Assess the background quality.
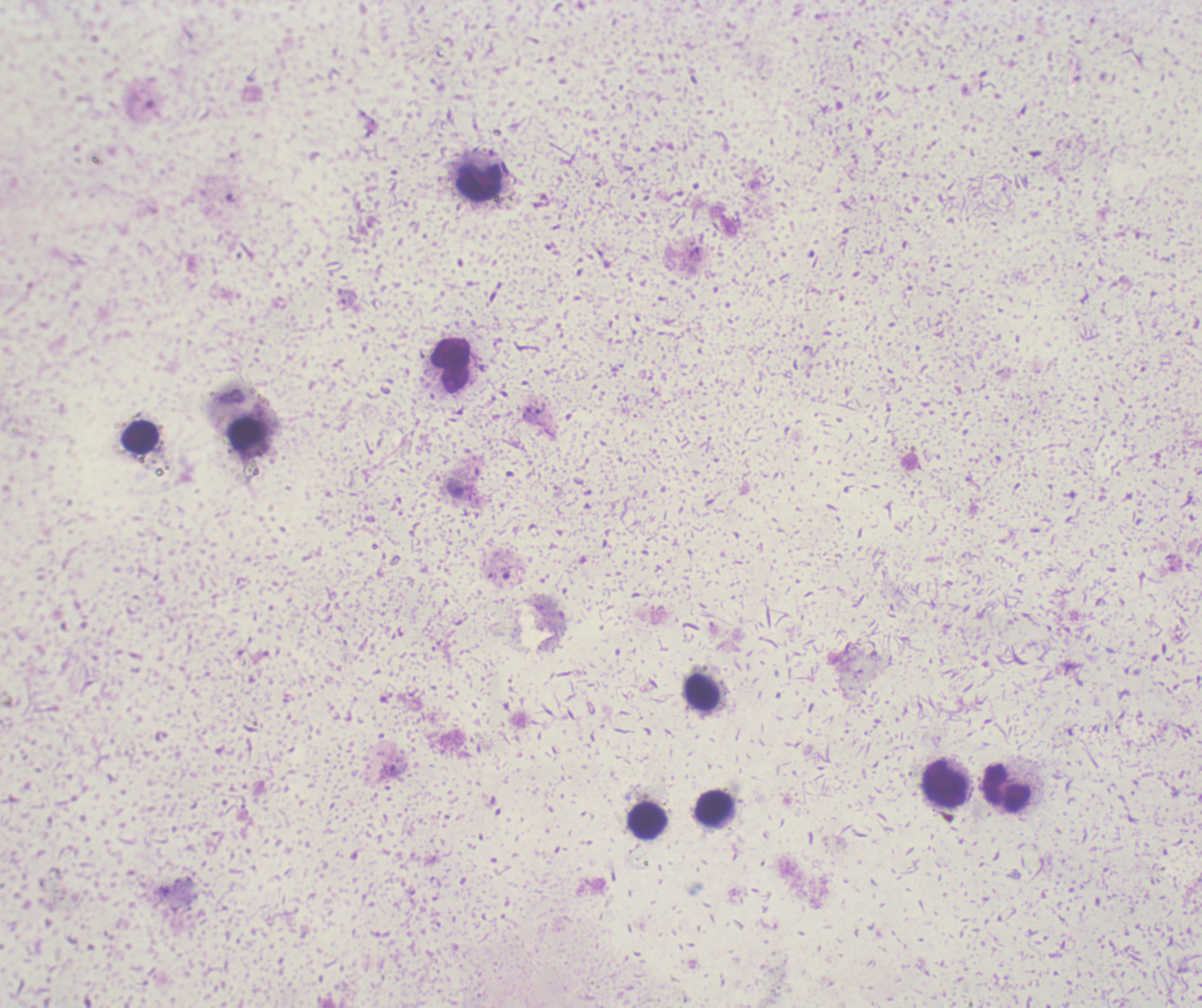

Unsatisfactory.

Approximate object centers, in pixels from the top-left corner. Trophozoite locations: (x=392, y=770). Leukocyte locations: (x=479, y=182), (x=451, y=364), (x=140, y=438), (x=702, y=692), (x=946, y=783), (x=1007, y=788), (x=714, y=807), (x=647, y=821). Thick blood film. Captured at 100x magnification. Previously used in an actual diagnosis. Romanowsky-stained preparation. Image is 1202×1008 pixels. One field from this slide. Result: positive for malaria parasites.